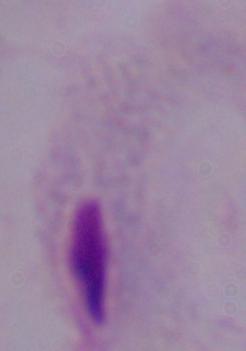
identification: trichomonad
magnification: 1000x
modality: photomicrograph